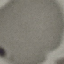

Summary:
  - Result: no malaria parasites detected
  - Image type: cell patch, automatically extracted from a larger field of view and resized to 64 × 64 pixels
  - Stain: Giemsa
  - Preparation: thin blood smear
  - Capture: smartphone through the microscope eyepiece